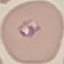
Malaria status: parasitized. Giemsa-stained preparation. Cell patch, automatically extracted from a larger field of view and resized to 64 × 64 pixels. Photographed with a smartphone camera at the microscope eyepiece. Thin blood film.